Assess this cell for malaria.
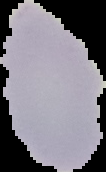
It is uninfected.

image type = segmented cell region on a black background
image size = 106×172 pixels
preparation = thin blood smear